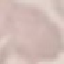

Summary:
  - Result: negative for malaria parasites
  - Preparation: thin blood smear
  - Stain: Giemsa
  - Capture: smartphone through the microscope eyepiece
  - Image type: automatically extracted cell patch, resized to 64 × 64 pixels